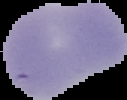
Result: negative for Plasmodium parasites. The area outside the segmented cell region is set to black. Image is 127×100 pixels. From a thin blood film.